Locate and identify every blood parasite.
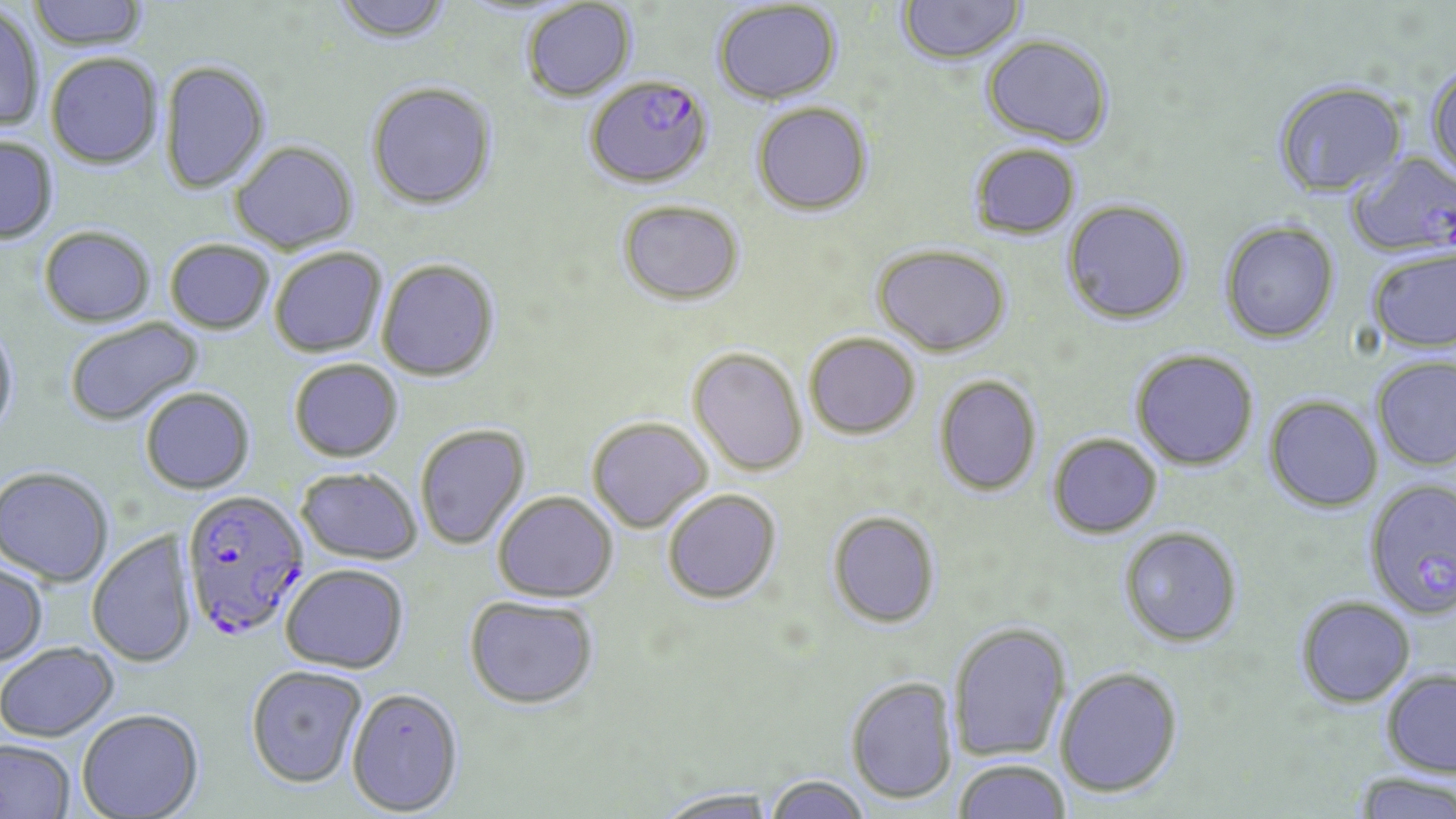
Approximate bounding boxes as [x1, y1, x2, y2] in pixels.
Plasmodium falciparum-infected red blood cells: [578, 77, 716, 192], [1345, 149, 1456, 259], [1371, 478, 1453, 622], [180, 490, 310, 642].
No Plasmodium ovale, Plasmodium malariae, Plasmodium vivax, Babesia divergens, or Trypanosoma brucei observed.

slide-level diagnosis = Plasmodium falciparum
magnification = 1000x
image size = 1456×819 pixels
stain = May-Grünwald-Giemsa
uninfected red blood cell locations = approximate bounding boxes as [x1, y1, x2, y2] in pixels: [28, 0, 148, 50], [330, 0, 456, 46], [896, 0, 1026, 66], [522, 1, 637, 102], [711, 2, 843, 105], [0, 4, 45, 132], [981, 34, 1115, 147], [46, 53, 163, 169], [159, 60, 271, 194], [1425, 64, 1456, 180], [1272, 80, 1407, 197], [366, 82, 498, 211], [751, 101, 873, 216], [0, 137, 58, 244], [230, 141, 359, 254], [967, 143, 1082, 239], [1061, 199, 1192, 325], [618, 200, 745, 307], [1219, 220, 1340, 344], [39, 226, 156, 328], [165, 240, 275, 335], [872, 243, 1011, 357], [1366, 247, 1456, 354], [270, 248, 387, 358], [376, 259, 500, 382], [64, 317, 205, 428], [0, 320, 20, 440], [805, 333, 921, 439], [687, 347, 808, 476], [1131, 348, 1258, 470], [1371, 356, 1456, 471], [289, 359, 403, 463], [934, 375, 1042, 496], [141, 388, 255, 495], [1264, 395, 1384, 512], [586, 417, 713, 534], [414, 424, 531, 550], [1048, 433, 1162, 538], [0, 467, 113, 586], [295, 469, 422, 564], [662, 488, 781, 603], [493, 491, 618, 602], [827, 510, 940, 627], [1119, 526, 1243, 646], [87, 530, 196, 669], [0, 563, 48, 667], [280, 565, 409, 674], [464, 594, 600, 710], [1295, 596, 1415, 707], [949, 621, 1072, 762], [0, 643, 119, 742], [245, 666, 367, 789], [1054, 666, 1183, 797], [1381, 668, 1456, 777], [846, 676, 958, 804], [347, 687, 465, 816], [77, 709, 206, 818], [0, 740, 75, 819], [954, 758, 1071, 819], [1351, 771, 1456, 818], [766, 774, 872, 819], [652, 787, 781, 818]
field of view = single
modality = light microscopy
preparation = thin blood smear